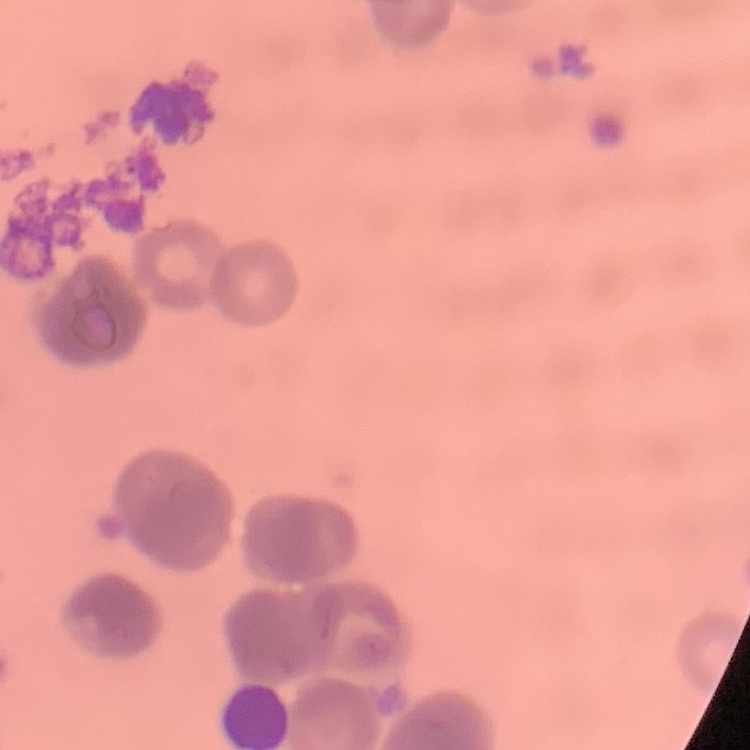
Summary:
  - Red blood cell morphology: rouleaux formation
  - Stain: Field's or Giemsa
  - Preparation: thin blood smear
  - Image type: square crop of a larger photomicrograph